Assess this cell for malaria.
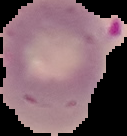

Parasitized.

{
  "image_size": "127×136 pixels",
  "image_type": "segmented cell region on a black background",
  "preparation": "thin blood smear"
}